Identify the parasite.
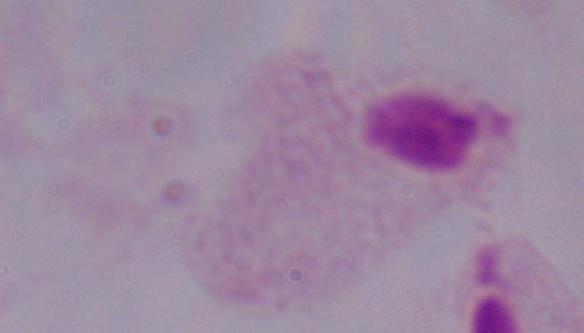

A trichomonad.

magnification = 1000x
modality = micrograph